Name the blood parasite species.
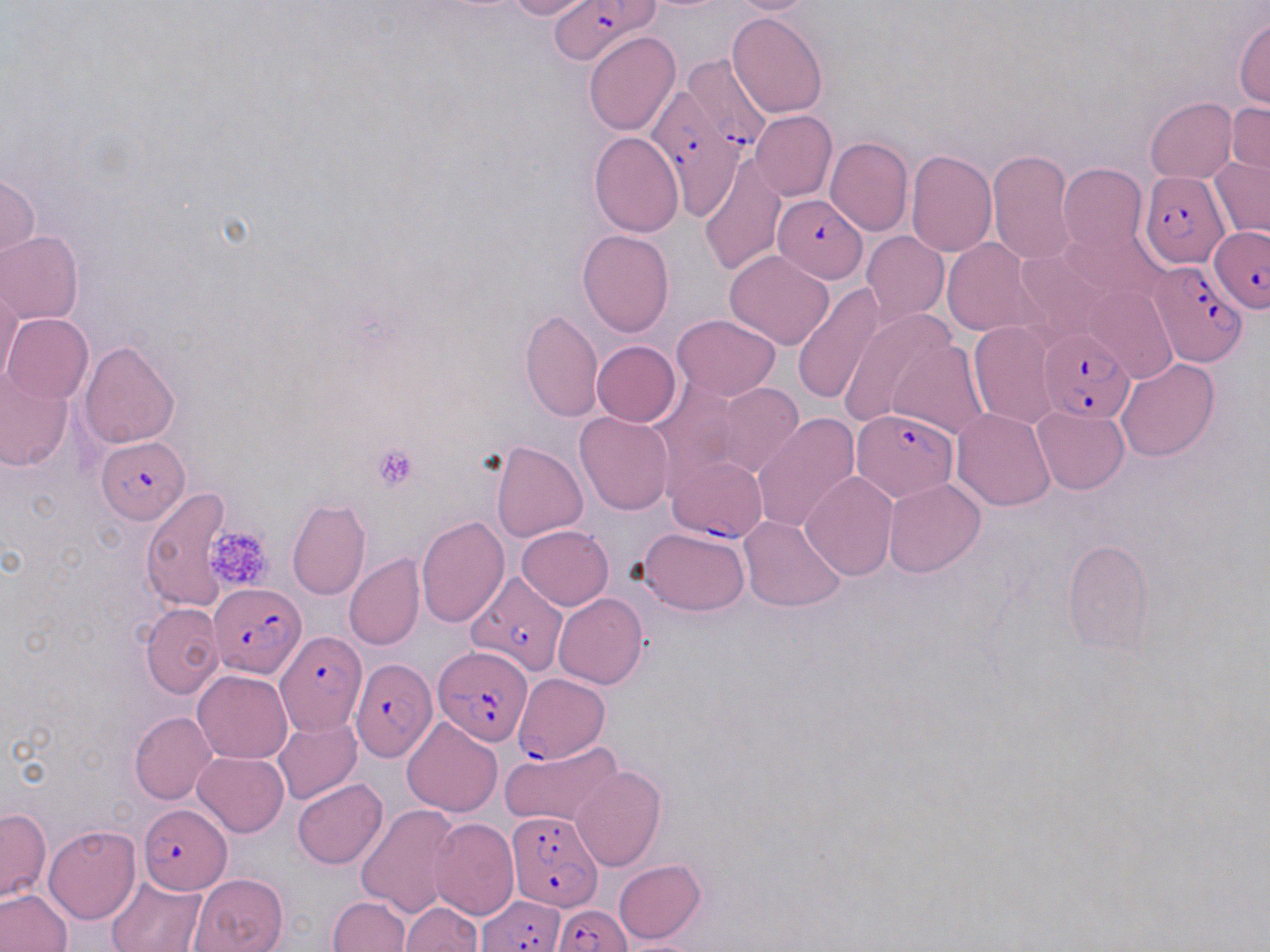
Plasmodium falciparum.

Approximate bounding boxes as (x1, y1, x2, y2) in pixels. Plasmodium falciparum-infected red blood cell locations: (546, 1, 655, 66), (681, 54, 773, 156), (647, 84, 746, 212), (1142, 170, 1229, 268), (772, 195, 867, 282), (1210, 226, 1270, 312), (1150, 260, 1249, 368), (1040, 328, 1135, 423), (853, 408, 957, 502), (96, 436, 188, 526), (667, 456, 768, 542), (470, 572, 573, 676), (210, 580, 303, 676), (275, 629, 366, 735), (433, 646, 533, 746), (349, 656, 433, 766), (512, 673, 610, 764), (137, 804, 232, 894), (506, 811, 603, 915), (474, 896, 565, 951), (552, 904, 632, 952). Platelet locations: (373, 445, 419, 490), (204, 524, 272, 593). Uninfected red blood cell locations: (503, 0, 596, 20), (727, 0, 816, 14), (727, 10, 828, 118), (1233, 17, 1270, 110), (584, 31, 680, 135), (1145, 97, 1236, 183), (1227, 102, 1270, 182), (751, 110, 837, 200), (589, 131, 683, 237), (825, 136, 913, 235), (905, 148, 997, 256), (986, 149, 1077, 265), (700, 150, 787, 276), (1208, 156, 1270, 239), (1057, 163, 1148, 256), (1, 174, 39, 264), (1058, 218, 1164, 306), (577, 229, 674, 336), (861, 230, 950, 325), (1, 231, 85, 325), (941, 237, 1040, 337), (1011, 248, 1113, 343), (725, 249, 836, 349), (790, 282, 882, 406), (0, 286, 21, 388), (1085, 286, 1176, 384), (837, 305, 954, 429), (520, 309, 603, 424), (3, 314, 93, 405), (670, 314, 782, 400), (968, 321, 1060, 430), (78, 339, 180, 448), (592, 341, 681, 427), (887, 342, 988, 440), (1116, 358, 1220, 461), (0, 371, 73, 471), (650, 378, 745, 485), (710, 381, 804, 480), (1032, 404, 1129, 495), (951, 408, 1056, 511), (751, 411, 859, 535), (574, 412, 674, 516), (490, 440, 588, 543), (800, 472, 898, 581), (883, 479, 985, 577), (141, 487, 233, 610), (286, 498, 370, 600), (416, 515, 509, 628), (738, 516, 845, 613), (517, 525, 613, 609), (637, 526, 750, 614), (1062, 539, 1155, 655), (344, 553, 425, 651), (553, 593, 648, 689), (140, 602, 224, 699), (193, 670, 293, 764), (129, 712, 217, 804), (402, 715, 504, 817), (274, 717, 362, 804), (499, 740, 624, 828), (193, 751, 289, 835), (571, 766, 666, 871), (292, 778, 387, 868), (356, 804, 460, 919), (0, 807, 52, 904), (428, 817, 518, 921), (42, 824, 140, 924), (613, 858, 707, 943), (189, 873, 288, 952), (105, 874, 206, 952), (0, 889, 72, 952), (327, 896, 410, 951), (399, 902, 482, 952). Thin blood film. Light microscopy. May-Grünwald-Giemsa-stained preparation. One field of a larger specimen. Image is 1270×952 pixels. 1000x magnification.